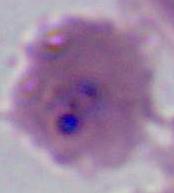

modality = photomicrograph
magnification = 400x or 1000x
identification = Plasmodium